Outline each blood parasite and name the species.
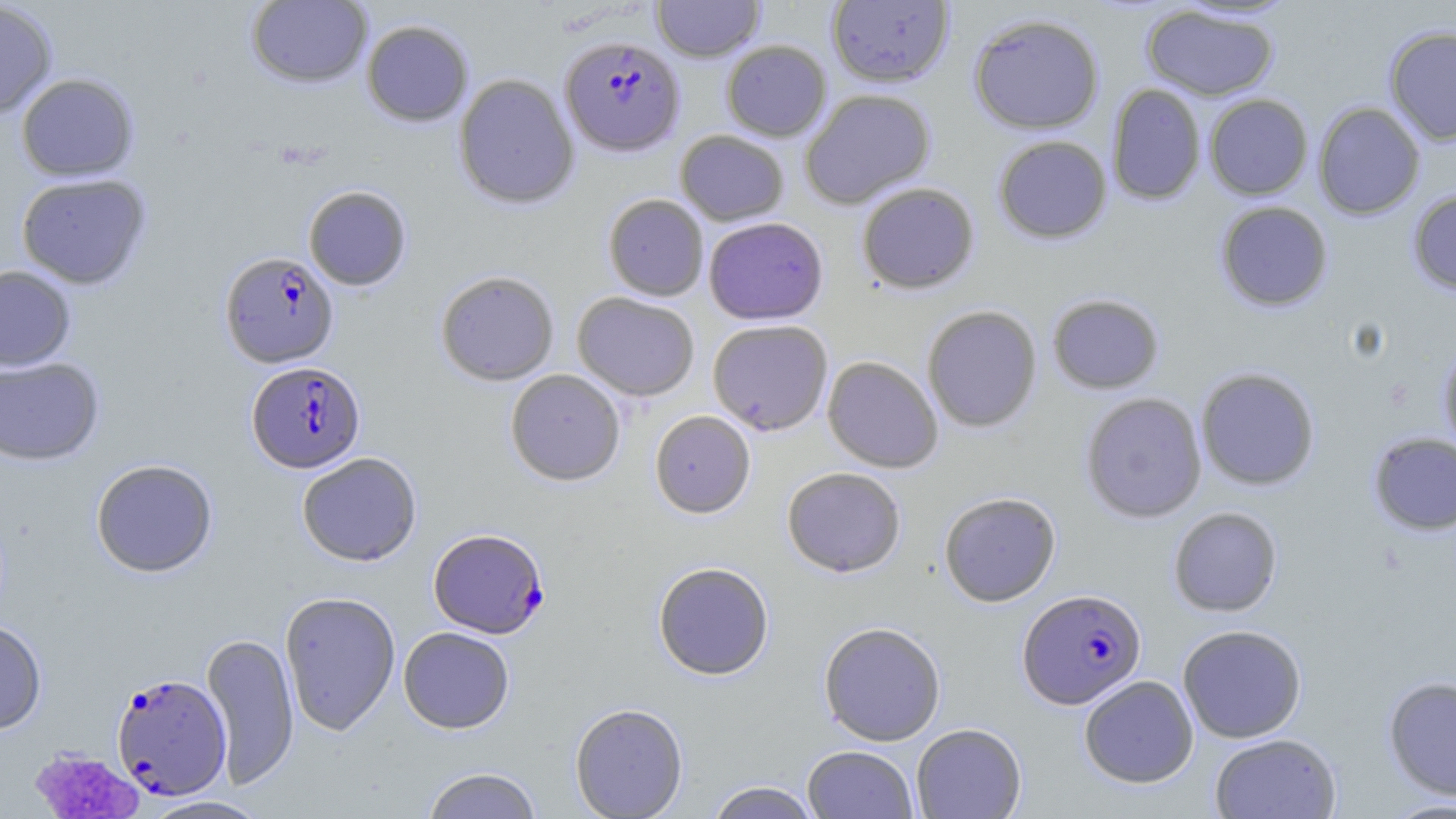

Approximate bounding boxes as (x1, y1, x2, y2) in pixels.
Plasmodium falciparum-infected red blood cells: (560, 35, 685, 156), (220, 252, 339, 368), (246, 361, 365, 473), (428, 527, 549, 638), (1017, 588, 1147, 709), (111, 673, 232, 799).
No Plasmodium ovale, Plasmodium malariae, Plasmodium vivax, Babesia divergens, or Trypanosoma brucei observed.

slide-level diagnosis = Plasmodium falciparum
modality = optical microscopy
platelet locations = approximate bounding boxes as (x1, y1, x2, y2) in pixels: (28, 746, 143, 819)
preparation = thin blood film
uninfected red blood cell locations = approximate bounding boxes as (x1, y1, x2, y2) in pixels: (246, 0, 373, 89), (651, 0, 764, 62), (0, 1, 58, 118), (826, 1, 954, 87), (1141, 4, 1280, 101), (968, 13, 1105, 135), (361, 20, 473, 127), (1384, 26, 1456, 145), (721, 40, 832, 141), (16, 73, 139, 181), (453, 73, 580, 210), (1107, 83, 1206, 205), (799, 89, 936, 208), (1204, 94, 1313, 200), (1312, 101, 1425, 220), (675, 129, 789, 225), (992, 135, 1112, 244), (16, 173, 152, 289), (856, 182, 980, 295), (303, 186, 412, 291), (1407, 189, 1456, 295), (603, 194, 709, 301), (1215, 201, 1333, 312), (703, 216, 828, 324), (0, 265, 76, 372), (435, 270, 559, 386), (572, 292, 700, 401), (1047, 292, 1165, 394), (921, 305, 1042, 432), (708, 319, 833, 435), (1437, 339, 1456, 458), (822, 356, 943, 473), (0, 357, 105, 466), (1195, 367, 1320, 491), (505, 369, 626, 486), (1079, 392, 1207, 523), (649, 410, 756, 518), (1367, 432, 1456, 536), (297, 452, 422, 566), (90, 459, 218, 578), (782, 466, 906, 577), (938, 491, 1061, 606), (1168, 506, 1283, 617), (653, 561, 774, 680), (279, 591, 401, 735), (0, 620, 47, 734), (818, 621, 946, 745), (1177, 624, 1307, 743), (398, 627, 515, 733), (201, 632, 299, 789), (1079, 675, 1199, 788), (1381, 675, 1456, 801), (569, 703, 689, 818), (911, 723, 1027, 819), (1209, 732, 1342, 819), (803, 745, 919, 819), (421, 767, 543, 819), (705, 781, 822, 819), (139, 795, 272, 819), (1379, 796, 1456, 819)
image size = 1456×819 pixels
field of view = one of a larger specimen
magnification = 1000x
stain = May-Grünwald-Giemsa